Assess this cell for malaria.
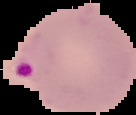
It is parasitized.

{
  "image_type": "segmented cell region with the area outside set to black",
  "image_size": "136×115 pixels",
  "preparation": "thin blood smear"
}